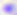

Summary:
  - Magnification: 400x
  - Identification: Toxoplasma gondii
  - Modality: micrograph